Report the malaria status of this cell.
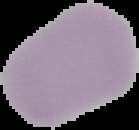
Uninfected.

image_size: 139×130 pixels
image_type: segmented cell region with the area outside set to black
preparation: thin blood film